Name the parasite shown.
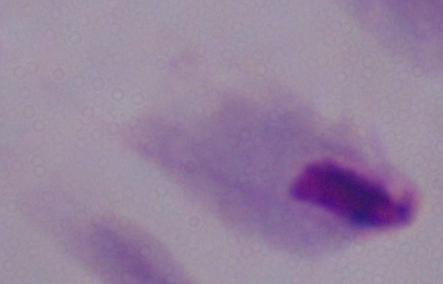

This is a trichomonad.

{
  "magnification": "1000x",
  "modality": "micrograph"
}